Give the position of every Plasmodium parasite.
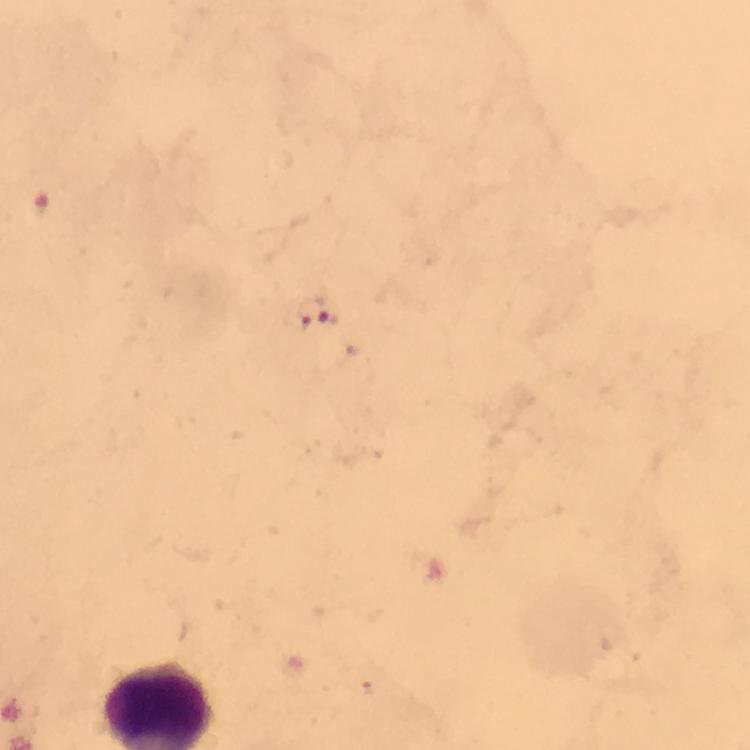

Approximate centers as {x, y} in pixels.
Plasmodium parasites: {315, 309}.

Summary:
  - Image size: 750×750 pixels
  - Stain: Giemsa
  - Preparation: thick blood smear
  - Immersion oil: used
  - Capture: smartphone camera through the microscope
  - Cropped from: one field of view
  - Magnification: 100x
  - Context: from a malaria diagnostic workup